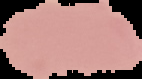
preparation: thin blood smear
image_size: 142×79 pixels
result: negative for malaria parasites
image_type: cell region segmented out of the field of view; surrounding area masked to black